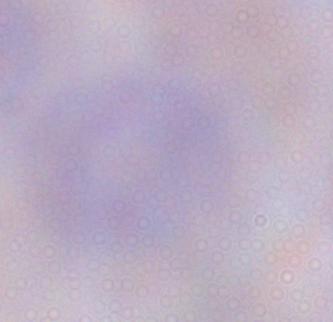
Summary:
  - Magnification: 1000x
  - Modality: micrograph
  - Identification: trypanosome